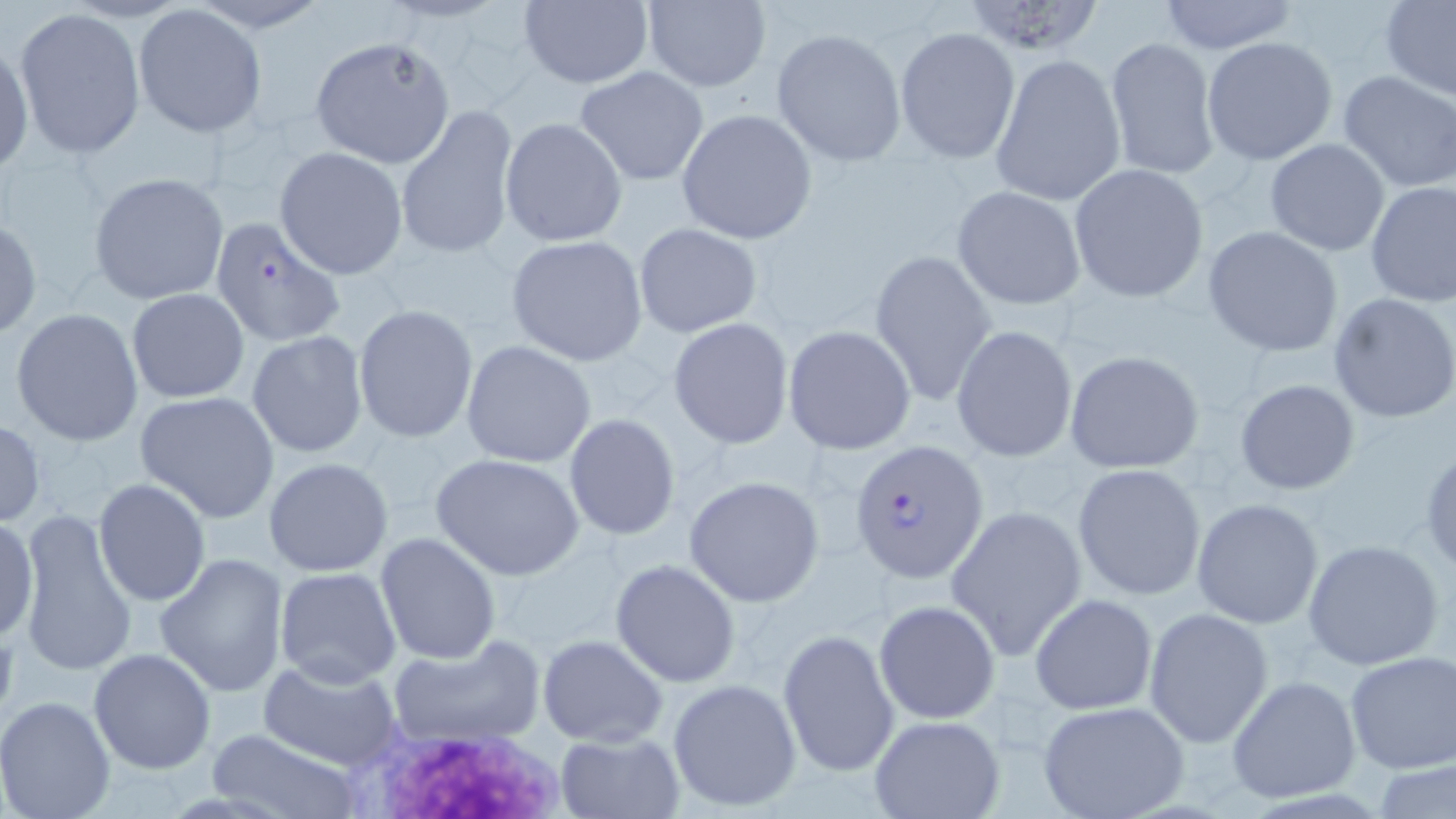

Plasmodium falciparum-infected red blood cell locations = approximate bounding boxes as [x1, y1, x2, y2] in pixels: [847, 438, 990, 583]
slide-level diagnosis = Plasmodium falciparum
magnification = 1000x
image size = 1456×819 pixels
modality = optical microscopy
platelet locations = approximate bounding boxes as [x1, y1, x2, y2] in pixels: [354, 721, 574, 817]
uninfected red blood cell locations = approximate bounding boxes as [x1, y1, x2, y2] in pixels: [189, 0, 334, 32], [518, 0, 654, 88], [1152, 0, 1302, 54], [640, 1, 771, 91], [957, 1, 1108, 56], [1380, 2, 1456, 100], [132, 4, 268, 138], [13, 9, 147, 160], [894, 26, 1021, 163], [771, 27, 908, 167], [1104, 36, 1220, 183], [309, 37, 456, 168], [1201, 37, 1338, 166], [0, 39, 33, 177], [989, 53, 1126, 207], [576, 66, 709, 186], [1338, 69, 1456, 194], [396, 105, 518, 262], [676, 108, 817, 245], [500, 117, 628, 248], [1265, 138, 1391, 256], [274, 147, 408, 280], [1068, 163, 1209, 303], [88, 171, 230, 306], [1363, 180, 1456, 305], [952, 186, 1086, 310], [209, 217, 348, 346], [0, 218, 42, 340], [632, 222, 763, 338], [1203, 226, 1346, 358], [505, 234, 649, 366], [871, 248, 998, 408], [126, 288, 251, 403], [1328, 293, 1456, 425], [352, 304, 479, 442], [9, 307, 145, 447], [669, 318, 794, 448], [950, 324, 1078, 463], [783, 325, 916, 455], [246, 332, 370, 459], [460, 340, 598, 468], [1064, 348, 1205, 475], [1233, 379, 1360, 496], [135, 390, 280, 523], [562, 413, 681, 542], [0, 418, 46, 528], [1420, 447, 1456, 577], [430, 453, 585, 579], [262, 456, 394, 578], [1072, 463, 1206, 601], [684, 475, 823, 607], [92, 479, 211, 606], [1192, 497, 1326, 629], [946, 505, 1087, 662], [12, 512, 138, 674], [1, 513, 38, 645], [374, 531, 503, 664], [1302, 538, 1443, 669], [154, 552, 289, 697], [610, 558, 742, 688], [273, 565, 404, 689], [1029, 593, 1158, 714], [875, 599, 1001, 723], [1143, 607, 1275, 748], [777, 630, 899, 779], [538, 634, 669, 746], [386, 635, 545, 748], [87, 648, 217, 774], [1343, 650, 1454, 775], [257, 659, 403, 771], [1227, 675, 1361, 804], [666, 677, 804, 814], [0, 695, 117, 819], [1038, 700, 1191, 819], [867, 714, 1005, 819], [204, 728, 362, 818], [554, 732, 686, 818]
preparation = thin blood smear
stain = May-Grünwald-Giemsa
field of view = one of a larger specimen